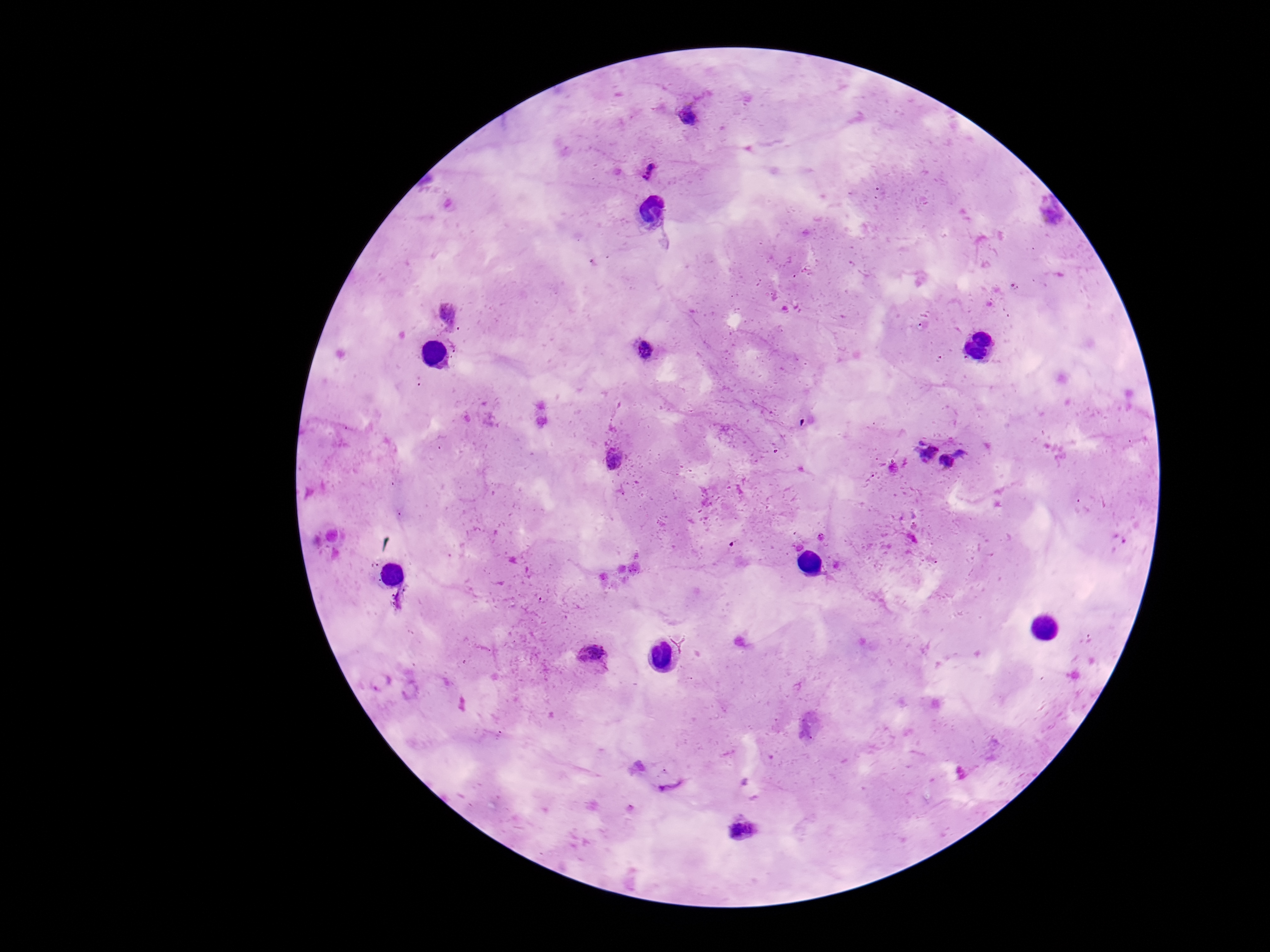

image_size: 1270×952 pixels
magnification: 100x
patient_malaria_status: positive
field_of_view: single
stain: Giemsa
plasmodium_parasite_locations: 'approximate object centers, in pixels from the top-left corner: (x=690, y=114), (x=648, y=168), (x=1050, y=217), (x=1015, y=286), (x=449, y=314), (x=646, y=350), (x=924, y=450), (x=613, y=460), (x=958, y=460), (x=594, y=654), (x=743, y=829)'
capture: smartphone camera through the microscope eyepiece
preparation: thick blood film